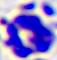

magnification: 400x
modality: photomicrograph
identification: white blood cell